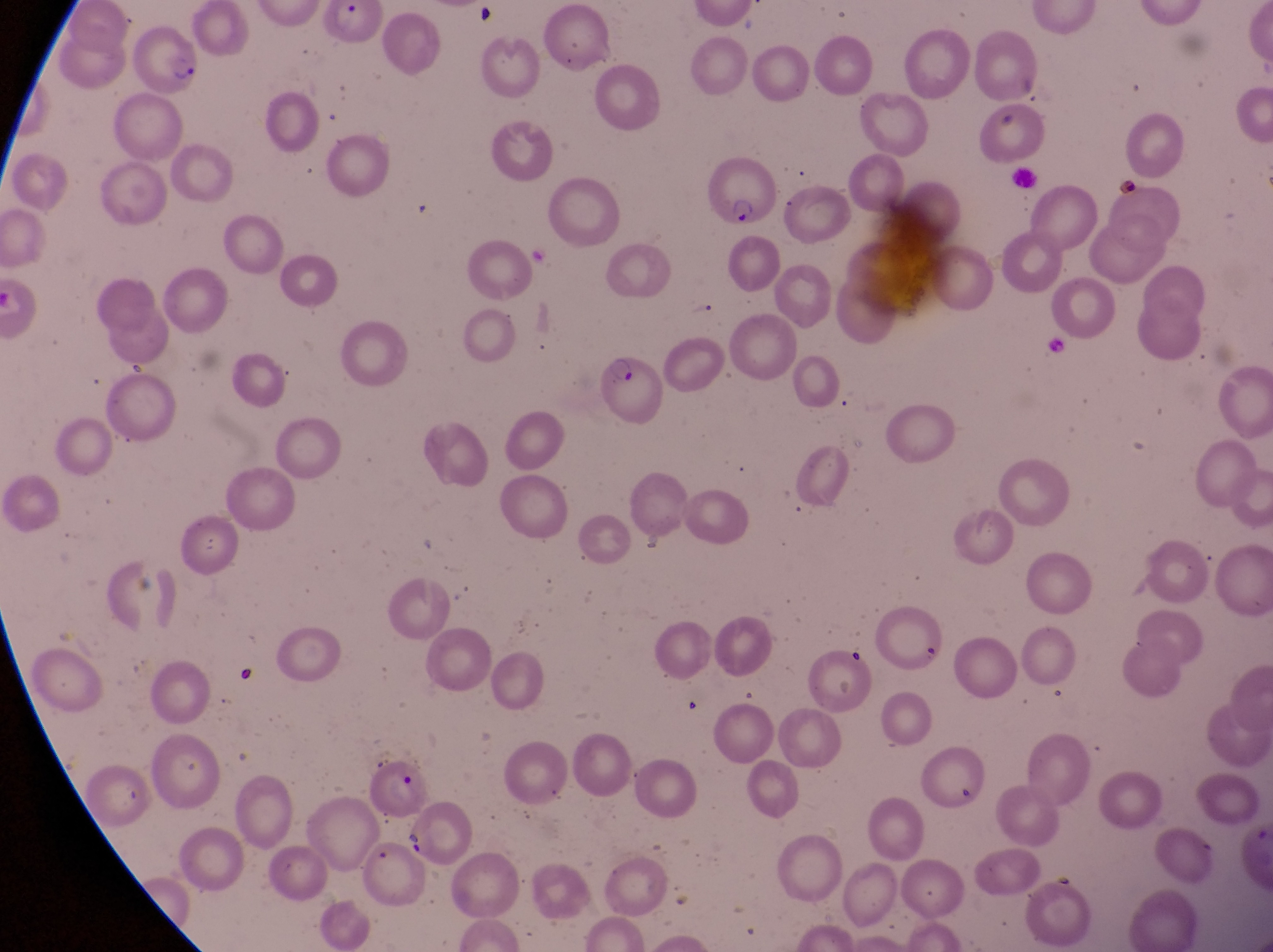

preparation = thin blood smear
capture = smartphone photograph through the eyepiece of an Olympus CX-23 microscope
parasitised red blood cell locations = approximate bounding boxes as [left, top, right, bottom] in pixels: [127, 24, 197, 90], [706, 157, 778, 222], [582, 348, 660, 425], [359, 756, 431, 821]
field of view = single
magnification = 1000x
image size = 1273×952 pixels
country = Uganda
artifact (platelet-like body, stain precipitate, or debris) locations = approximate bounding boxes as [left, top, right, bottom] in pixels: [996, 102, 1023, 130], [402, 826, 425, 858]